Assess the morphology of the erythrocytes.
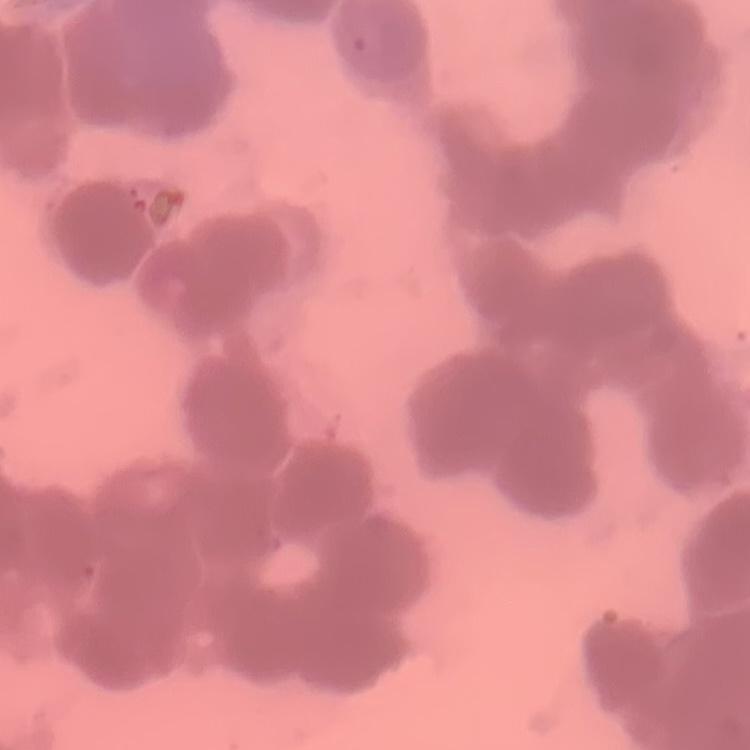
They show rouleaux formation.

preparation = thin peripheral smear
image type = one tile cut from a larger photomicrograph
stain = Field's or Giemsa